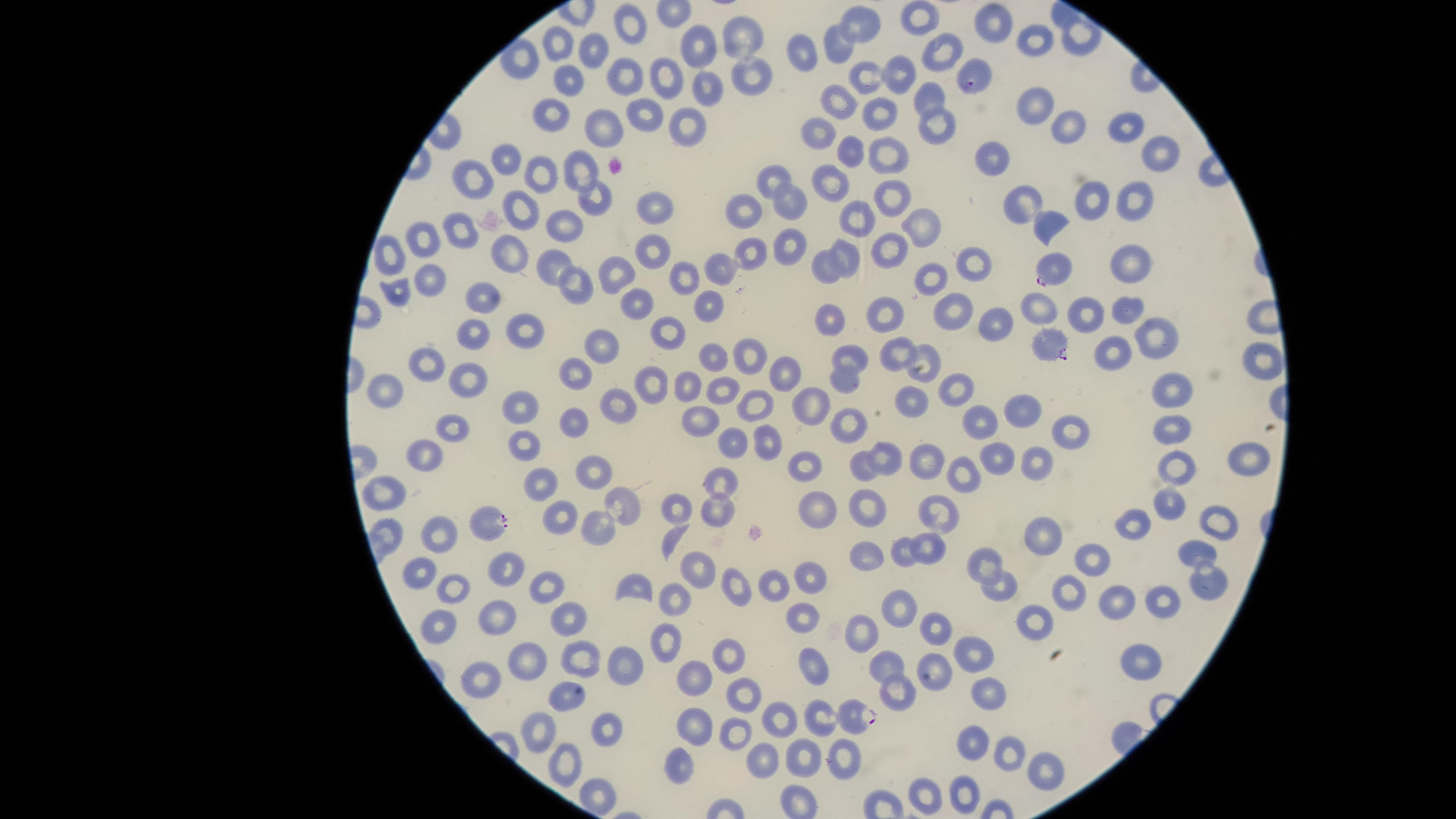

field of view = single
parasitized red blood cells = approximate marker points as [x, y] in pixels: [972, 77], [1048, 271], [1047, 342], [493, 524], [856, 714]
image size = 1456×819 pixels
capture = smartphone photograph through the microscope eyepiece
species = Plasmodium falciparum
stain = Giemsa
presence = malaria parasites detected
uninfected red blood cells = approximate marker points as [x, y] in pixels: [919, 16], [627, 18], [863, 24], [995, 24], [742, 39], [1032, 42], [707, 44], [559, 46], [837, 46], [1079, 46], [593, 49], [940, 50], [803, 53], [901, 72], [625, 73], [749, 77], [872, 77], [566, 79], [660, 81], [706, 91], [929, 98], [1034, 102], [842, 103], [877, 114], [647, 117], [555, 120], [1066, 126], [604, 128], [689, 128], [938, 128], [1122, 128], [822, 133], [1157, 151], [851, 153], [503, 154], [884, 156], [993, 161], [540, 173], [580, 175], [775, 179], [477, 181], [834, 187], [891, 197], [1092, 199], [1137, 200], [1029, 202], [594, 203], [789, 205], [519, 209], [652, 209], [742, 213], [859, 219], [923, 224], [564, 225], [1046, 227], [460, 234], [424, 242], [790, 244], [652, 251], [891, 251], [848, 254], [394, 258], [756, 258], [507, 261], [977, 263], [1130, 263], [718, 264], [552, 266], [826, 268], [616, 277], [685, 277], [933, 277], [430, 281], [578, 288], [396, 291], [486, 300], [640, 304], [1039, 309], [709, 311], [952, 313], [1091, 313], [1127, 313], [890, 314], [833, 325], [994, 328], [520, 330], [477, 337], [1151, 339], [667, 340], [602, 348], [897, 350], [925, 351], [1111, 353], [714, 355], [759, 357], [1256, 357], [853, 359], [426, 362], [575, 373], [786, 375], [463, 376], [848, 380], [649, 384], [723, 389], [696, 390], [956, 391], [1171, 395], [389, 396], [913, 404], [522, 405], [618, 405], [752, 407], [809, 407], [1012, 413], [699, 417], [577, 420], [848, 424], [979, 424], [454, 427], [1175, 428], [1068, 429], [766, 442], [733, 445], [527, 449], [882, 457], [420, 459], [996, 459], [1039, 460], [1248, 460], [808, 461], [1183, 464], [931, 465], [598, 468], [867, 469], [965, 473], [538, 484], [722, 485], [396, 499], [626, 501], [1174, 501], [682, 510], [719, 510], [817, 510], [866, 513], [563, 514], [938, 514], [595, 524], [1138, 524], [1218, 524], [439, 534], [384, 536], [1046, 539], [675, 541], [903, 549], [929, 549], [1196, 556], [876, 559], [1094, 561], [699, 565], [986, 565], [506, 570], [423, 574], [811, 574], [1209, 579], [456, 584], [543, 584], [733, 586], [1002, 587], [640, 588], [775, 590], [1070, 592], [900, 594], [678, 601], [1122, 605], [1171, 605], [807, 617], [497, 618], [572, 618], [1034, 618], [440, 627], [938, 638], [861, 639], [666, 645], [1142, 650], [975, 654], [728, 658], [527, 664], [579, 664], [626, 668], [815, 670], [887, 672], [482, 677], [694, 679], [989, 690], [564, 694], [742, 695], [891, 701], [780, 718], [822, 721], [733, 728], [538, 729], [608, 729], [696, 729], [973, 738], [766, 750], [1008, 752], [842, 758], [808, 761], [566, 762], [679, 764], [1040, 774], [596, 792], [964, 794], [921, 795]
preparation = thin blood film
visible region = circular